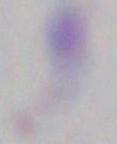

Toxoplasma gondii is shown. Photomicrograph. 1000x magnification.